Assess the morphology of the red blood cells.
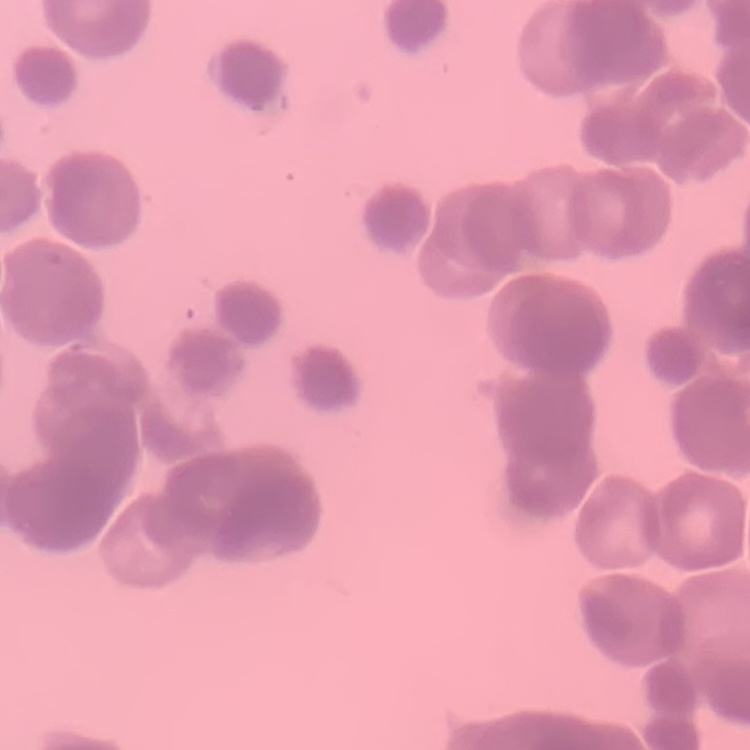
Rouleaux formation.

One tile cut from a larger photomicrograph. Stained with either Field's or Giemsa. Thin blood film.